State the blood parasite species.
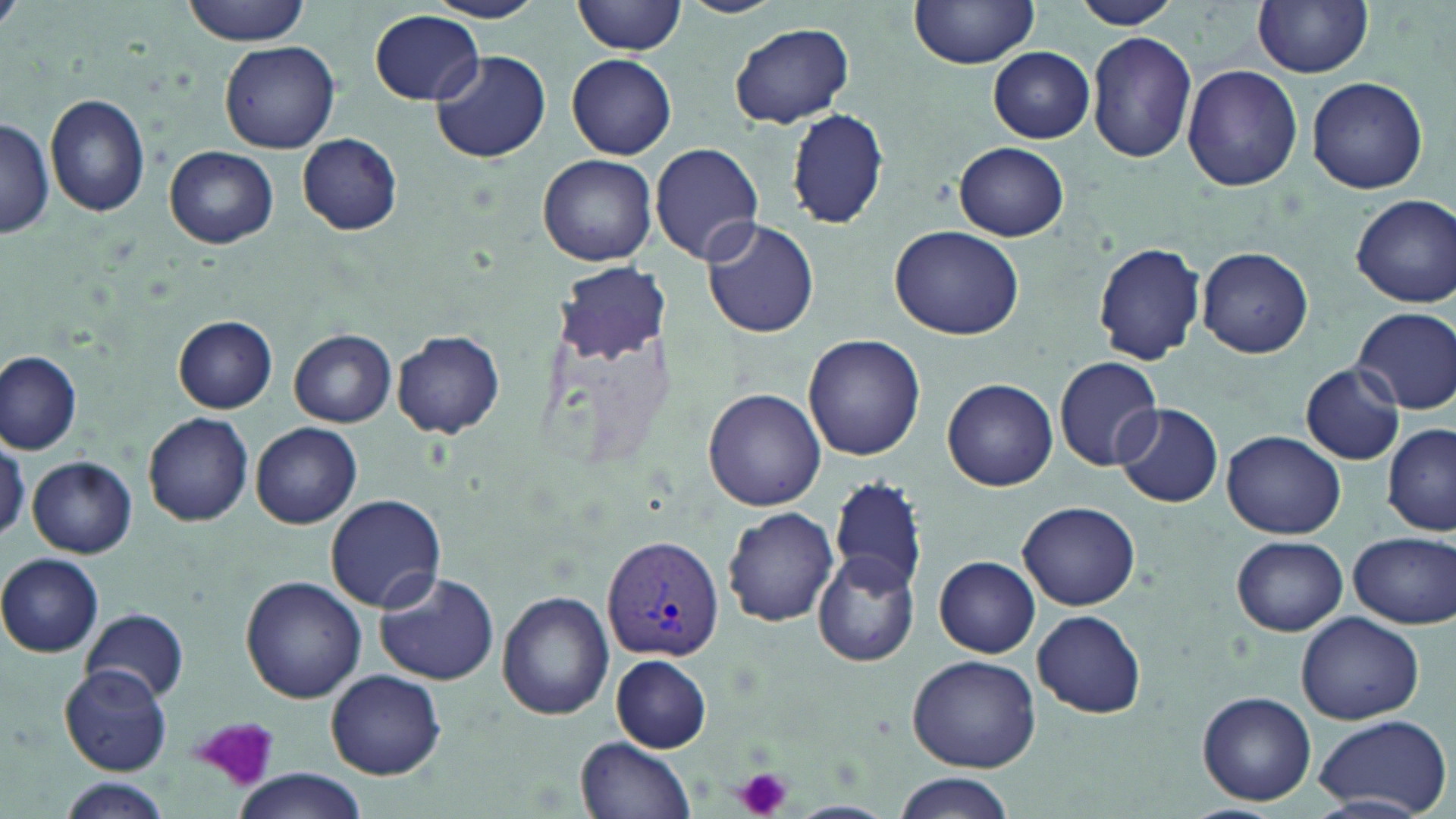

Plasmodium vivax.

field_of_view: one of a larger specimen
plasmodium_vivax_infected_red_blood_cell_locations: 'approximate bounding boxes as (x1,y1)-(x2,y2) corner pairs in pixels: (602,533)-(725,661)'
uninfected_red_blood_cell_locations: 'approximate bounding boxes as (x1,y1)-(x2,y2) corner pairs in pixels: (182,0)-(311,44), (424,0)-(546,24), (573,0)-(690,56), (909,0)-(1040,69), (1070,0)-(1180,29), (1253,0)-(1374,78), (369,9)-(483,107), (730,23)-(854,127), (1086,30)-(1198,163), (220,38)-(340,154), (989,47)-(1095,143), (429,49)-(550,163), (567,55)-(676,159), (1181,65)-(1302,191), (1306,76)-(1429,194), (46,94)-(151,218), (786,106)-(889,230), (0,117)-(55,240), (297,134)-(403,235), (650,142)-(765,265), (953,142)-(1068,241), (164,146)-(278,248), (538,154)-(658,266), (1352,194)-(1455,307), (700,216)-(820,338), (889,225)-(1025,341), (1094,241)-(1207,364), (1198,247)-(1313,358), (557,260)-(666,364), (1353,308)-(1455,413), (173,315)-(278,413), (289,329)-(395,426), (392,331)-(505,438), (803,334)-(925,461), (0,352)-(83,455), (1054,356)-(1164,470), (1300,363)-(1405,465), (942,378)-(1058,492), (704,388)-(827,510), (1114,402)-(1224,508), (142,412)-(253,526), (250,421)-(362,529), (1382,425)-(1455,535), (1221,431)-(1347,540), (0,434)-(28,543), (27,456)-(137,557), (827,476)-(928,594), (324,495)-(446,611), (1017,500)-(1142,609), (721,506)-(839,626), (1347,530)-(1455,629), (1232,536)-(1348,636), (813,551)-(919,668), (0,552)-(103,657), (935,555)-(1041,656), (371,571)-(499,686), (239,574)-(366,704), (497,591)-(613,720), (82,607)-(189,704), (1032,611)-(1145,715), (1295,613)-(1424,726), (907,653)-(1041,772), (611,654)-(713,752), (60,667)-(172,775), (326,669)-(447,779), (1197,691)-(1316,805), (1312,712)-(1451,816), (577,736)-(695,818), (232,770)-(369,819), (892,774)-(1019,819), (61,780)-(173,819)'
platelet_locations: 'approximate bounding boxes as (x1,y1)-(x2,y2) corner pairs in pixels: (189,716)-(286,789), (736,767)-(793,818)'
magnification: 1000x
modality: optical microscopy
preparation: thin blood film
stain: May-Grünwald-Giemsa
image_size: 1456×819 pixels